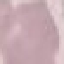

Result: no malaria parasites seen. Giemsa stain. Acquired by smartphone through the microscope eyepiece. Cell patch, automatically extracted from a larger field of view and resized to 64 × 64 pixels. Thin smear of blood.